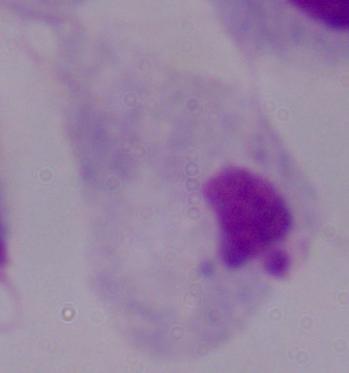

Micrograph. A trichomonad is shown. 1000x magnification.